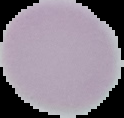

preparation = thin blood smear
image type = segmented cell region on a black background
malaria status = uninfected
image size = 124×118 pixels